Point out each leukocyte.
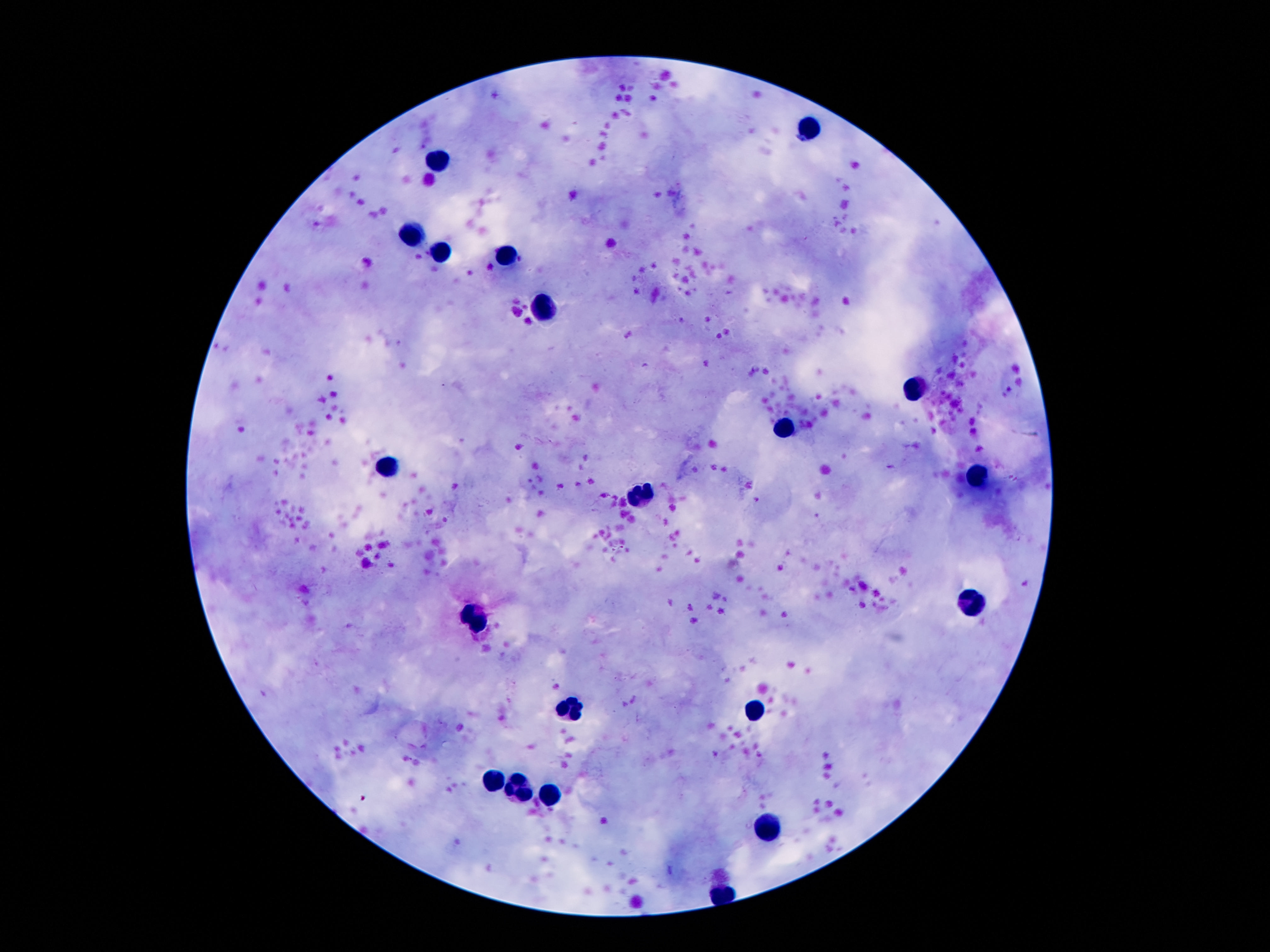

Approximate centers as [x, y] in pixels.
Leukocytes: [807, 130], [438, 158], [409, 231], [440, 250], [506, 256], [546, 309], [913, 388], [785, 429], [387, 469], [978, 477], [641, 494], [975, 602], [478, 615], [571, 708], [756, 708], [495, 779], [520, 789], [551, 796], [770, 825].

field of view = single
capture = smartphone camera through the microscope eyepiece
image size = 1270×952 pixels
preparation = thick blood smear
patient malaria status = uninfected
magnification = 100x
stain = Giemsa